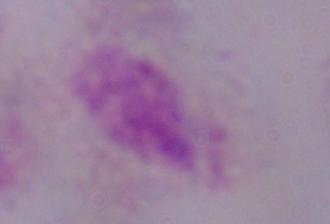

magnification = 1000x
identification = trichomonad
modality = micrograph